Locate and identify every blood parasite.
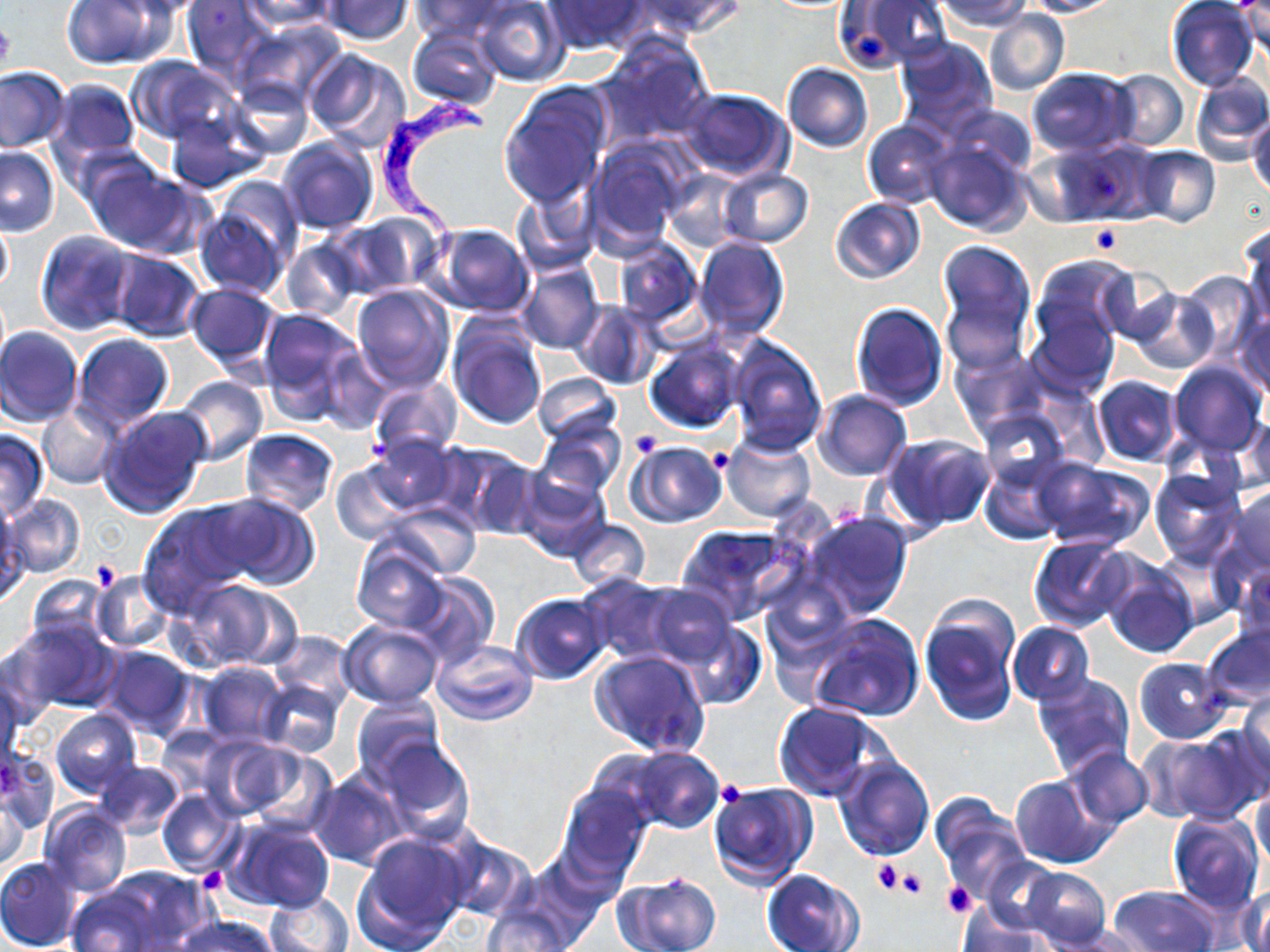

Approximate bounding boxes as (x1,y1)-(x2,y2) corner pairs in pixels.
Trypanosoma brucei: (373,84)-(487,280).
No Plasmodium falciparum, Plasmodium ovale, Plasmodium malariae, Plasmodium vivax, or Babesia divergens observed.

Summary:
  - Uninfected red blood cell locations: (62,0)-(166,69), (120,0)-(210,19), (182,0)-(275,80), (239,0)-(339,33), (321,0)-(414,44), (412,0)-(507,41), (472,0)-(568,86), (634,0)-(744,39), (837,0)-(952,72), (937,0)-(1031,32), (1024,0)-(1118,16), (544,1)-(648,54), (1166,1)-(1257,90), (1238,5)-(1268,56), (984,10)-(1069,96), (235,21)-(347,109), (407,27)-(503,110), (597,35)-(716,147), (894,35)-(997,136), (302,48)-(409,151), (126,56)-(234,145), (782,63)-(872,152), (0,66)-(71,152), (1027,66)-(1137,157), (1108,70)-(1189,152), (1188,72)-(1270,163), (226,76)-(313,158), (53,80)-(139,163), (499,86)-(611,208), (677,87)-(792,181), (949,104)-(1035,181), (164,110)-(267,194), (1249,111)-(1270,199), (863,119)-(954,208), (277,135)-(378,235), (924,135)-(1034,237), (586,140)-(687,250), (1037,142)-(1151,226), (1132,145)-(1221,227), (0,147)-(59,236), (84,160)-(205,259), (663,168)-(746,252), (718,168)-(813,249), (212,172)-(305,268), (510,183)-(599,276), (830,197)-(923,283), (194,205)-(287,297), (333,214)-(442,298), (1,217)-(13,296), (428,223)-(534,318), (1242,225)-(1270,331), (35,230)-(134,336), (693,236)-(791,343), (283,238)-(364,320), (935,240)-(1037,364), (613,242)-(703,328), (104,250)-(205,342), (1031,253)-(1137,347), (515,260)-(604,355), (1099,266)-(1180,343), (1177,270)-(1261,360), (184,282)-(280,368), (351,283)-(454,392), (1130,288)-(1219,374), (1026,298)-(1122,395), (850,301)-(948,409), (573,302)-(658,389), (256,308)-(358,417), (1233,312)-(1270,399), (447,317)-(547,431), (0,327)-(84,428), (71,334)-(174,433), (727,336)-(826,455), (644,339)-(745,433), (318,345)-(399,432), (951,347)-(1049,431), (1168,361)-(1266,457), (532,373)-(620,446), (173,374)-(267,466), (1092,376)-(1182,466), (366,378)-(462,460), (814,390)-(912,480), (37,404)-(121,488), (96,404)-(210,520), (978,409)-(1070,490), (1240,415)-(1270,493), (533,418)-(626,503), (0,428)-(51,520), (240,428)-(339,516), (369,434)-(460,515), (722,434)-(815,521), (886,436)-(995,529), (624,440)-(727,528), (438,441)-(542,539), (981,458)-(1068,545), (1032,459)-(1155,551), (331,462)-(414,544), (512,468)-(611,562), (1149,468)-(1243,567), (1224,486)-(1270,576), (208,493)-(320,589), (5,495)-(86,579), (138,500)-(256,612), (382,501)-(482,580), (0,507)-(25,600), (802,511)-(914,621), (567,518)-(651,592), (677,523)-(806,625), (1029,536)-(1137,631), (352,542)-(448,632), (1102,561)-(1198,659), (1234,565)-(1270,650), (92,572)-(175,653), (407,572)-(498,667), (576,574)-(678,663), (23,577)-(111,655), (177,578)-(298,672), (643,583)-(739,669), (510,592)-(612,684), (919,596)-(1021,728), (807,613)-(925,721), (7,618)-(118,715), (339,620)-(443,707), (677,622)-(766,709), (1007,622)-(1095,705), (1202,623)-(1270,710), (268,630)-(356,709), (1011,633)-(1111,756), (430,637)-(539,725), (1,639)-(47,734), (94,645)-(199,740), (591,648)-(710,756), (1135,657)-(1232,744), (196,661)-(289,748), (0,671)-(23,768), (1031,672)-(1135,779), (258,679)-(345,758), (1237,690)-(1270,784), (351,696)-(446,784), (774,702)-(885,801), (49,710)-(142,798), (156,726)-(230,797), (1149,728)-(1265,825), (371,736)-(474,842), (207,737)-(326,827), (626,747)-(722,832), (1063,747)-(1154,832), (1,751)-(58,833), (833,753)-(935,859), (93,759)-(184,839), (307,771)-(408,870), (1009,774)-(1110,868), (709,782)-(817,887), (1251,782)-(1270,876), (558,784)-(652,883), (0,785)-(27,878), (156,789)-(245,877), (931,797)-(1030,897), (39,805)-(132,896), (1167,810)-(1264,913), (222,817)-(336,915), (352,833)-(471,952), (438,835)-(534,922), (0,855)-(81,951), (1022,866)-(1110,949), (761,868)-(864,952), (65,870)-(201,952), (615,873)-(721,952), (1237,886)-(1270,952), (1109,887)-(1219,952), (261,891)-(357,952), (480,898)-(581,952), (956,903)-(1051,952), (172,915)-(279,952)
  - Platelet locations: (0,19)-(16,75), (855,31)-(889,61), (1088,226)-(1123,254), (632,431)-(664,458), (710,450)-(733,473), (89,563)-(120,591), (717,781)-(745,806), (872,858)-(903,894), (202,868)-(225,891), (895,869)-(930,900), (942,881)-(975,918)
  - Slide-level diagnosis: Trypanosoma brucei
  - Preparation: thin blood film
  - Magnification: 1000x
  - Stain: May-Grünwald-Giemsa
  - Modality: light microscopy
  - Field of view: one of a larger specimen
  - Image size: 1270×952 pixels